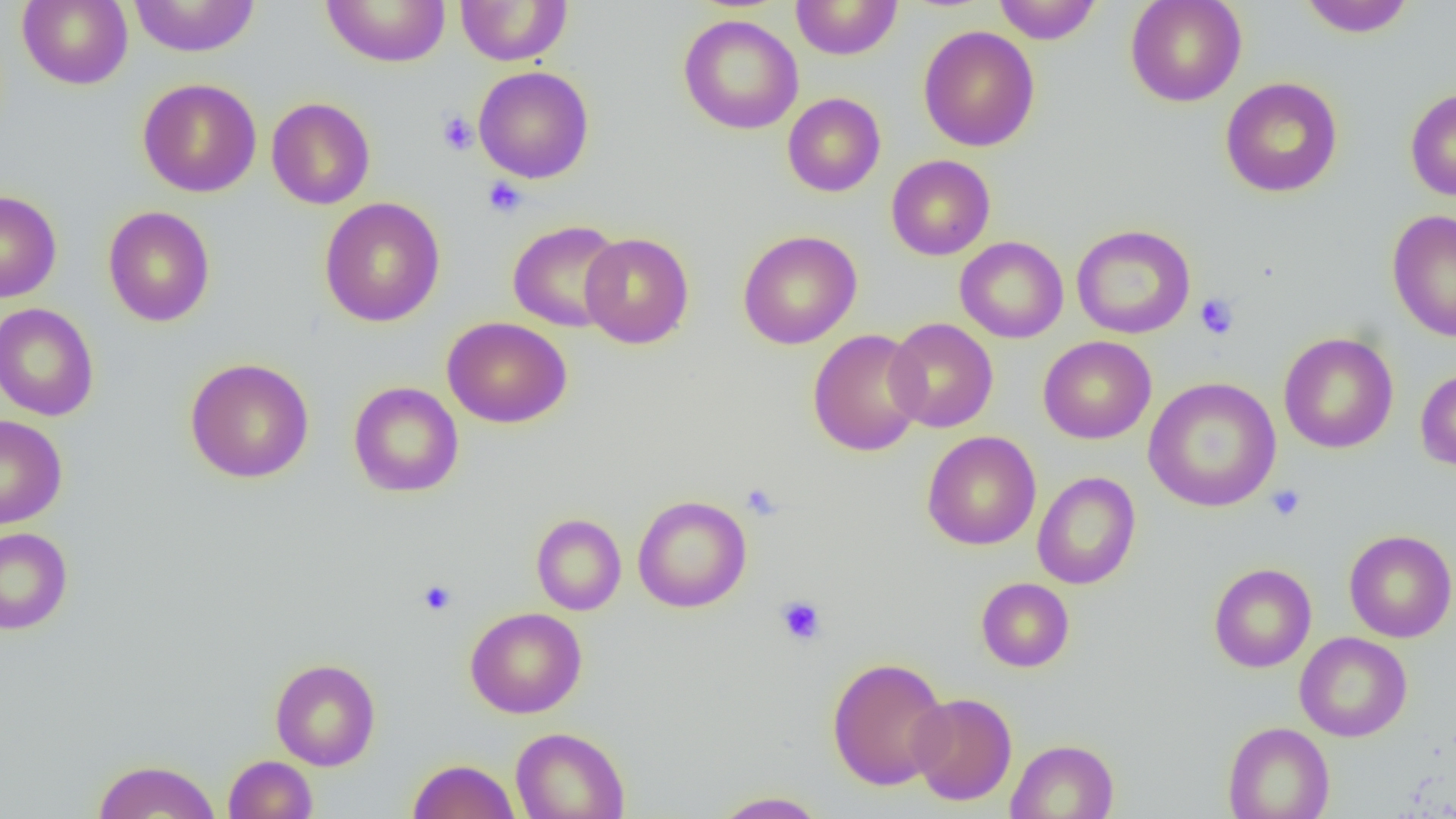
slide-level diagnosis = negative for blood parasites
image size = 1456×819 pixels
platelet locations = approximate bounding boxes as [x1, y1, x2, y2] in pixels: [437, 111, 478, 156], [483, 177, 527, 218], [1195, 293, 1239, 340], [741, 484, 782, 521], [1266, 485, 1305, 521], [417, 580, 457, 616], [775, 596, 826, 645]
modality = optical microscopy
preparation = thin blood smear
uninfected red blood cell locations = approximate bounding boxes as [x1, y1, x2, y2] in pixels: [18, 0, 133, 89], [128, 0, 261, 57], [321, 0, 450, 67], [455, 0, 572, 66], [790, 0, 903, 60], [993, 0, 1102, 44], [1125, 0, 1247, 107], [1298, 0, 1415, 38], [678, 14, 803, 135], [918, 26, 1040, 152], [474, 66, 594, 184], [1220, 77, 1343, 197], [138, 78, 262, 197], [1405, 88, 1456, 201], [782, 92, 885, 197], [266, 97, 375, 210], [886, 155, 995, 260], [0, 190, 61, 303], [320, 197, 446, 328], [102, 206, 215, 327], [1387, 209, 1456, 342], [507, 220, 626, 333], [1070, 224, 1196, 339], [738, 230, 862, 350], [579, 232, 694, 349], [955, 236, 1069, 343], [0, 303, 99, 421], [442, 317, 572, 428], [885, 317, 998, 433], [807, 329, 927, 456], [1278, 332, 1398, 453], [1038, 336, 1156, 444], [185, 358, 314, 483], [1415, 368, 1456, 472], [1143, 377, 1282, 512], [348, 381, 464, 497], [0, 415, 67, 529], [922, 431, 1041, 550], [1032, 471, 1141, 590], [633, 495, 752, 613], [531, 513, 626, 616], [0, 527, 73, 635], [1344, 529, 1456, 643], [1208, 563, 1317, 672], [976, 577, 1075, 672], [465, 607, 586, 718], [1295, 632, 1412, 742], [827, 656, 951, 791], [270, 658, 380, 771], [908, 692, 1018, 806], [1222, 721, 1335, 819], [510, 726, 631, 819], [1006, 738, 1120, 819], [223, 755, 318, 819], [407, 758, 520, 819], [92, 759, 221, 818], [710, 790, 830, 818]
magnification = 1000x
field of view = single